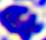
identification = leukocyte
modality = photomicrograph
magnification = 400x